Give the position of every malaria parasite.
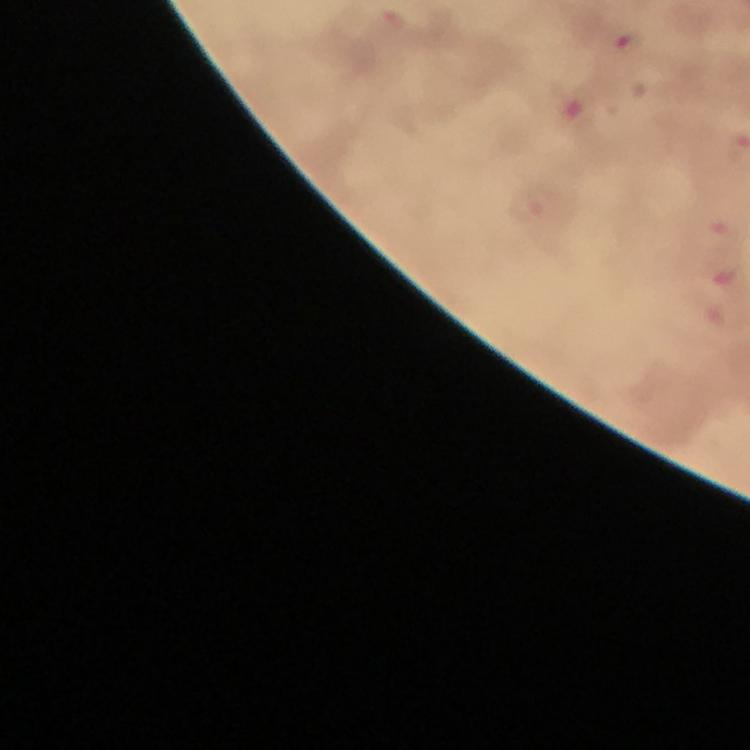

Approximate centers as (x, y) in pixels.
Malaria parasites: (625, 43), (531, 206), (718, 230).

{
  "capture": "smartphone photograph through a microscope",
  "context": "from a malaria diagnostic workup",
  "image_size": "750×750 pixels",
  "preparation": "thick blood smear",
  "magnification": "100x",
  "stain": "Giemsa",
  "cropped_from": "one field of view",
  "immersion_oil": "used"
}